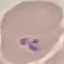
Summary:
  - Malaria status: parasitized
  - Stain: Giemsa
  - Image type: cell patch, automatically extracted from a larger field of view and resized to 64 × 64 pixels
  - Capture: smartphone camera at the microscope eyepiece
  - Preparation: thin blood film